Describe the morphology of the erythrocytes.
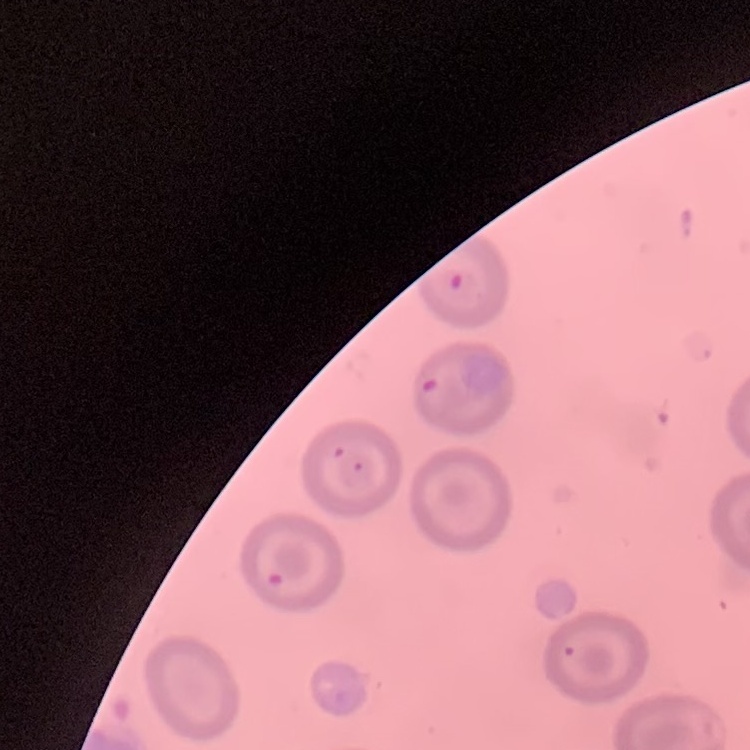
They show no rouleaux formation.

Thin blood film. Stained with either Field's or Giemsa. One tile cut from a larger photomicrograph.